State the blood parasite species.
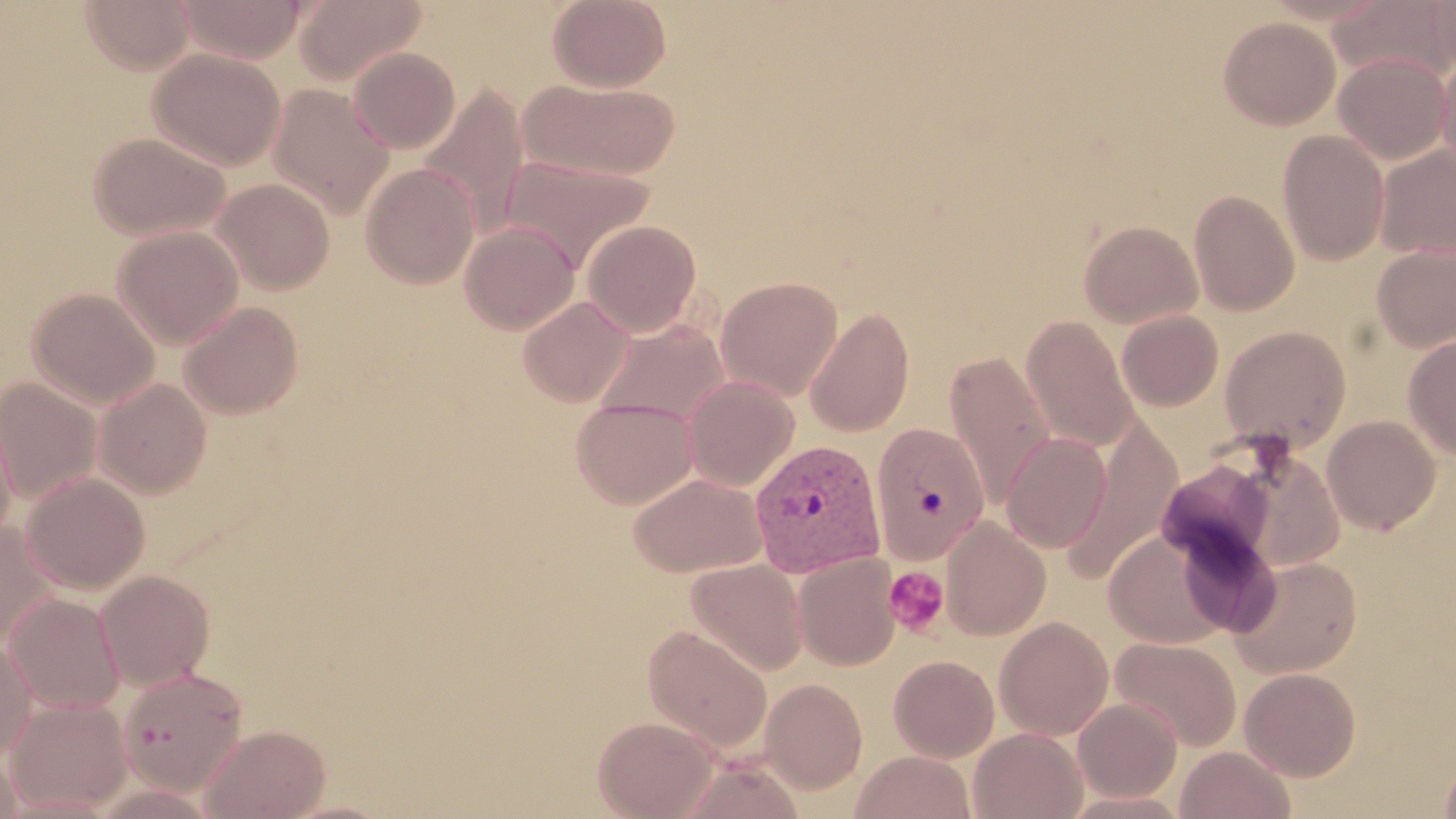

Plasmodium vivax.

magnification = 1000x
modality = light microscopy
uninfected red blood cell locations = approximate bounding boxes as [x1, y1, x2, y2] in pixels: [79, 0, 194, 73], [174, 0, 309, 63], [294, 0, 426, 85], [547, 0, 671, 91], [1328, 0, 1456, 85], [1429, 0, 1456, 76], [1217, 16, 1340, 130], [347, 47, 460, 153], [149, 48, 286, 170], [1437, 50, 1456, 177], [1333, 53, 1452, 165], [518, 78, 682, 182], [419, 84, 530, 240], [267, 85, 393, 218], [1277, 130, 1390, 266], [88, 131, 232, 241], [1375, 145, 1456, 259], [501, 154, 655, 272], [360, 162, 480, 289], [212, 178, 336, 296], [1189, 190, 1299, 316], [581, 220, 702, 337], [1079, 220, 1203, 328], [459, 221, 580, 335], [112, 225, 244, 350], [1372, 242, 1456, 352], [715, 275, 843, 401], [27, 288, 160, 408], [517, 296, 635, 407], [178, 301, 303, 419], [805, 306, 914, 436], [1116, 310, 1223, 412], [1021, 316, 1140, 453], [592, 318, 730, 428], [1219, 326, 1351, 452], [1403, 333, 1456, 459], [944, 351, 1056, 506], [682, 375, 799, 491], [0, 377, 103, 504], [94, 379, 211, 499], [571, 397, 699, 508], [0, 402, 18, 545], [1322, 415, 1441, 535], [1059, 416, 1183, 582], [871, 422, 993, 566], [1000, 432, 1112, 553], [21, 472, 150, 594], [628, 472, 768, 578], [939, 517, 1051, 641], [0, 522, 59, 649], [1104, 528, 1230, 649], [793, 553, 900, 670], [1229, 555, 1363, 678], [686, 559, 808, 675], [95, 570, 215, 690], [3, 592, 125, 715], [994, 616, 1114, 740], [642, 624, 773, 753], [0, 635, 36, 761], [1110, 637, 1242, 751], [888, 655, 999, 763], [1239, 667, 1361, 781], [118, 668, 247, 793], [759, 678, 868, 794], [3, 696, 133, 814], [1072, 698, 1182, 802], [592, 715, 721, 819], [200, 723, 331, 819], [969, 727, 1088, 819], [1175, 745, 1296, 819], [1438, 748, 1456, 819], [0, 749, 23, 818], [850, 750, 976, 819], [677, 757, 806, 819]
image size = 1456×819 pixels
stain = May-Grünwald-Giemsa
preparation = thin blood smear
platelet locations = approximate bounding boxes as [x1, y1, x2, y2] in pixels: [883, 566, 950, 638]
field of view = one of a larger specimen
Plasmodium vivax-infected red blood cell locations = approximate bounding boxes as [x1, y1, x2, y2] in pixels: [749, 439, 886, 577]